Describe the morphology of the red blood cells.
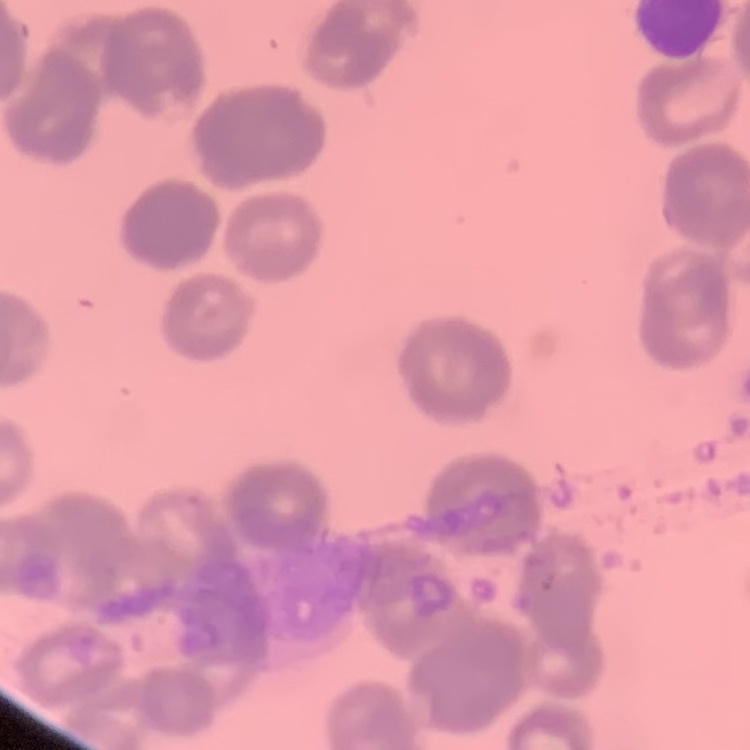
They show rouleaux formation.

One tile cut from a larger photomicrograph. Field's or Giemsa stain. Thin peripheral smear.